Assess this cell for malaria.
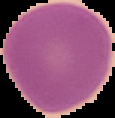

Uninfected.

Image is 115×118 pixels. Segmented cell region on a black background. From a thin blood film.